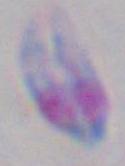

modality = micrograph
identification = Toxoplasma gondii
magnification = 1000x